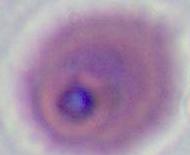
magnification: 400x or 1000x
modality: photomicrograph
identification: Plasmodium